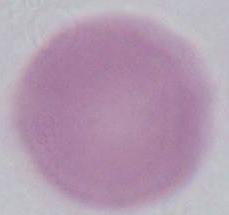 An erythrocyte is shown. Micrograph. 1000x magnification.